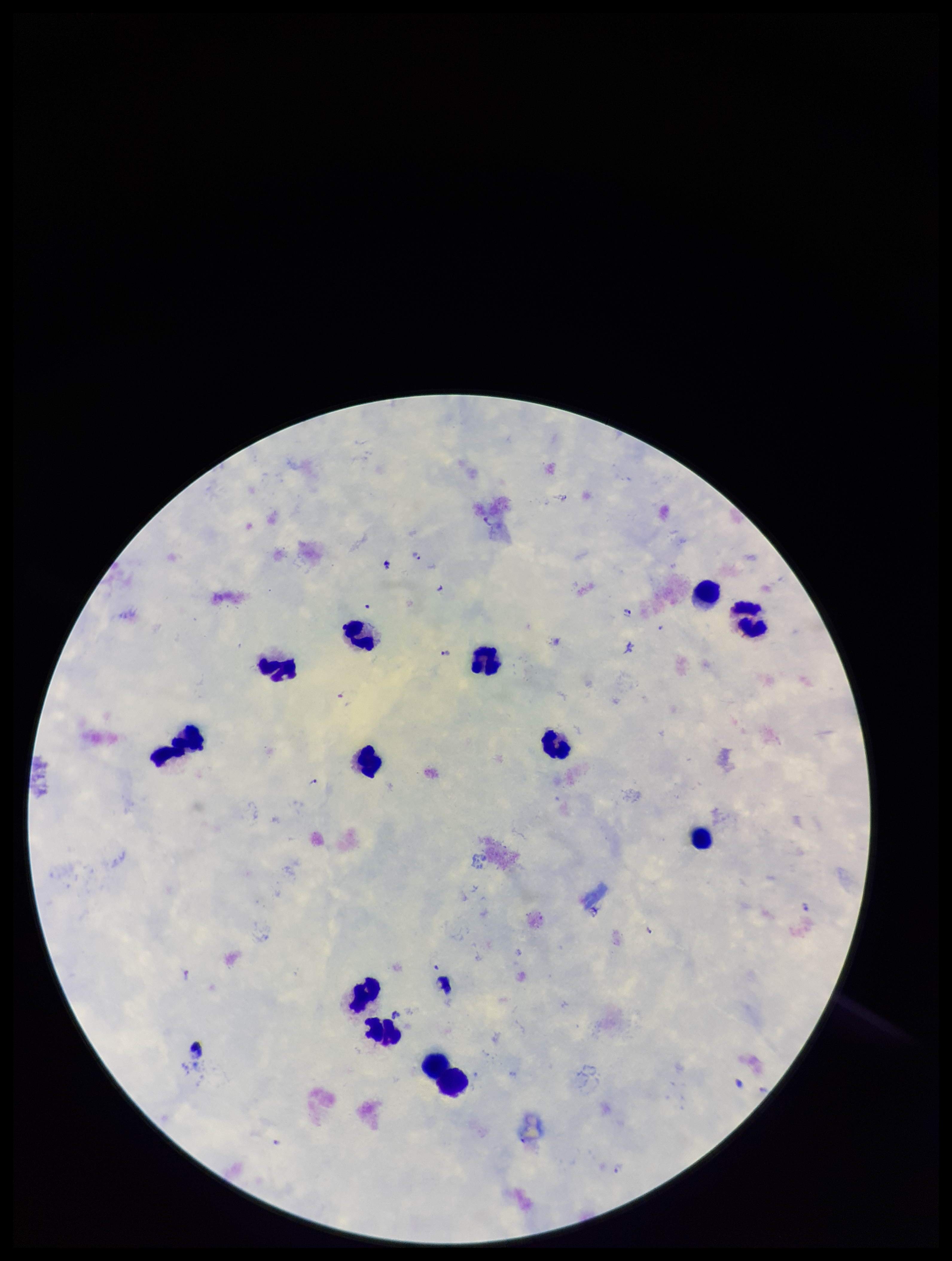

Patient malaria status: infected. Parasite count: 6. One field from this slide. Giemsa stain. Image is 952×1261 pixels. Leukocyte count: 12. Plasmodium parasites: identified. Species reported for this patient: Plasmodium falciparum. Smartphone photograph taken through the eyepiece of a microscope. Preparation: thick.